Identify the parasite.
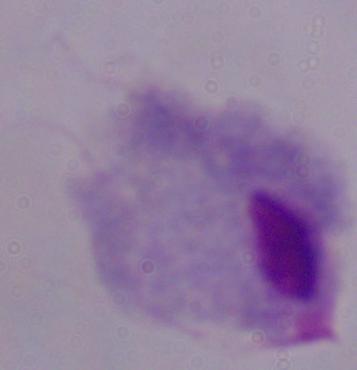

This is a trichomonad.

Photomicrograph. 1000x magnification.